Report the malaria status of this cell.
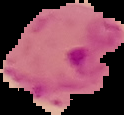

It is parasitized.

image size = 124×115 pixels
preparation = thin blood smear
image type = cell region segmented out of the field of view; surrounding area masked to black